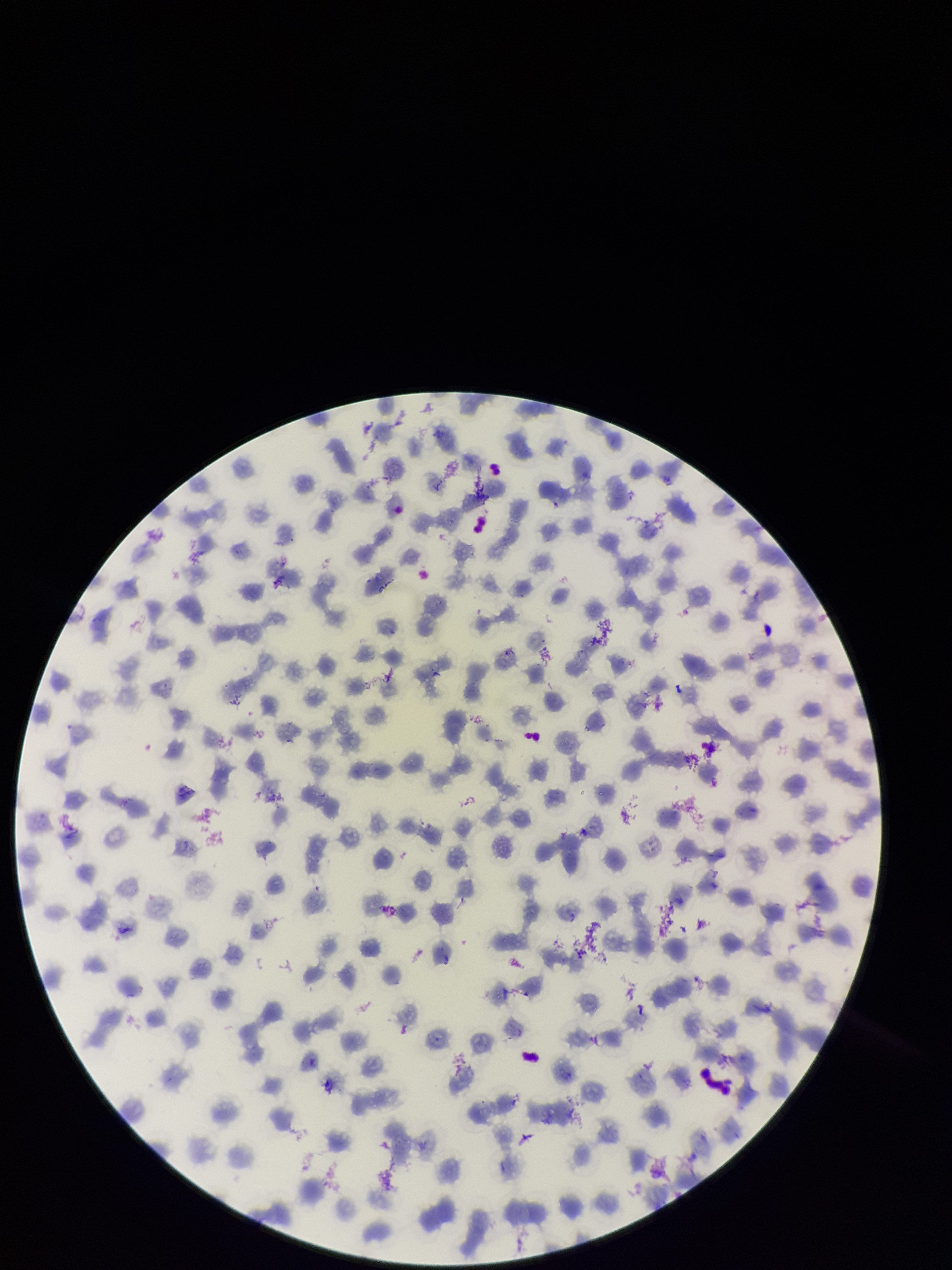
stain = Giemsa
field of view = one from this slide
patient malaria status = positive
species reported for this patient = Plasmodium falciparum
preparation = thin smear
capture = smartphone photograph through the microscope eyepiece
parasitized red blood cells = none seen
image size = 952×1270 pixels
red blood cell count = 178
parasitized red blood cell count = 0